Name the parasite shown.
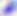

This is Toxoplasma gondii.

Photomicrograph. Captured at 400x magnification.